Outline each Plasmodium falciparum-infected red blood cell.
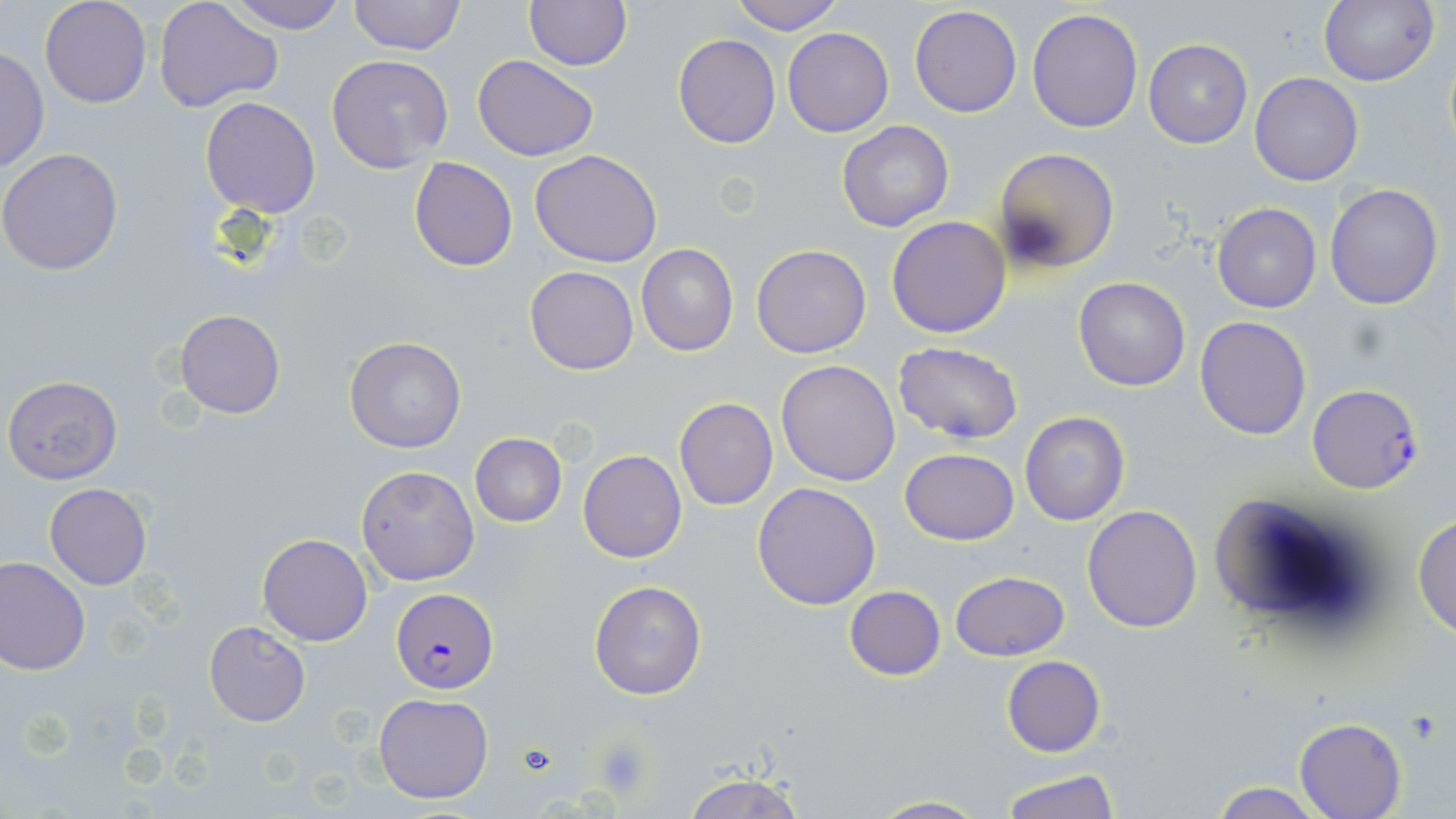

Approximate bounding boxes as (x1, y1, x2, y2) in pixels.
Plasmodium falciparum-infected red blood cells: (1307, 382, 1427, 494), (390, 588, 498, 693).

Platelet locations: (593, 736, 653, 801), (514, 742, 559, 779). Uninfected red blood cell locations: (153, 0, 285, 115), (224, 0, 351, 32), (348, 0, 466, 56), (729, 0, 845, 34), (1319, 0, 1438, 87), (39, 1, 151, 109), (524, 1, 631, 70), (910, 4, 1022, 118), (1027, 8, 1143, 132), (784, 27, 893, 137), (673, 33, 779, 149), (1143, 38, 1252, 149), (1, 45, 49, 176), (329, 54, 454, 173), (473, 55, 599, 162), (1250, 72, 1363, 186), (201, 97, 321, 219), (838, 121, 954, 233), (994, 147, 1119, 274), (0, 148, 125, 277), (531, 149, 662, 266), (409, 157, 518, 272), (1324, 183, 1444, 310), (1212, 202, 1323, 313), (886, 216, 1011, 338), (637, 244, 738, 357), (751, 244, 872, 358), (525, 265, 639, 376), (1073, 276, 1191, 392), (173, 309, 286, 418), (1194, 315, 1313, 440), (344, 337, 466, 453), (894, 342, 1023, 444), (775, 359, 901, 486), (4, 375, 124, 484), (674, 397, 779, 510), (1019, 411, 1131, 526), (469, 433, 568, 527), (899, 448, 1019, 544), (578, 450, 686, 563), (357, 464, 479, 585), (44, 481, 153, 589), (752, 482, 881, 610), (1209, 495, 1346, 616), (1083, 504, 1202, 632), (1413, 513, 1455, 640), (258, 533, 371, 646), (0, 557, 91, 676), (951, 570, 1070, 660), (589, 580, 706, 700), (845, 586, 946, 680), (205, 622, 310, 726), (1001, 656, 1105, 757), (372, 693, 494, 805), (1294, 717, 1407, 818), (682, 766, 804, 819), (999, 767, 1120, 818), (1204, 780, 1325, 818), (866, 794, 990, 818). Slide-level diagnosis: Plasmodium falciparum. Thin blood film. Captured at 1000x magnification. May-Grünwald-Giemsa-stained preparation. Image is 1456×819 pixels. Single field of view. Light microscopy.